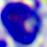
A leukocyte is shown. 400x magnification. Micrograph.